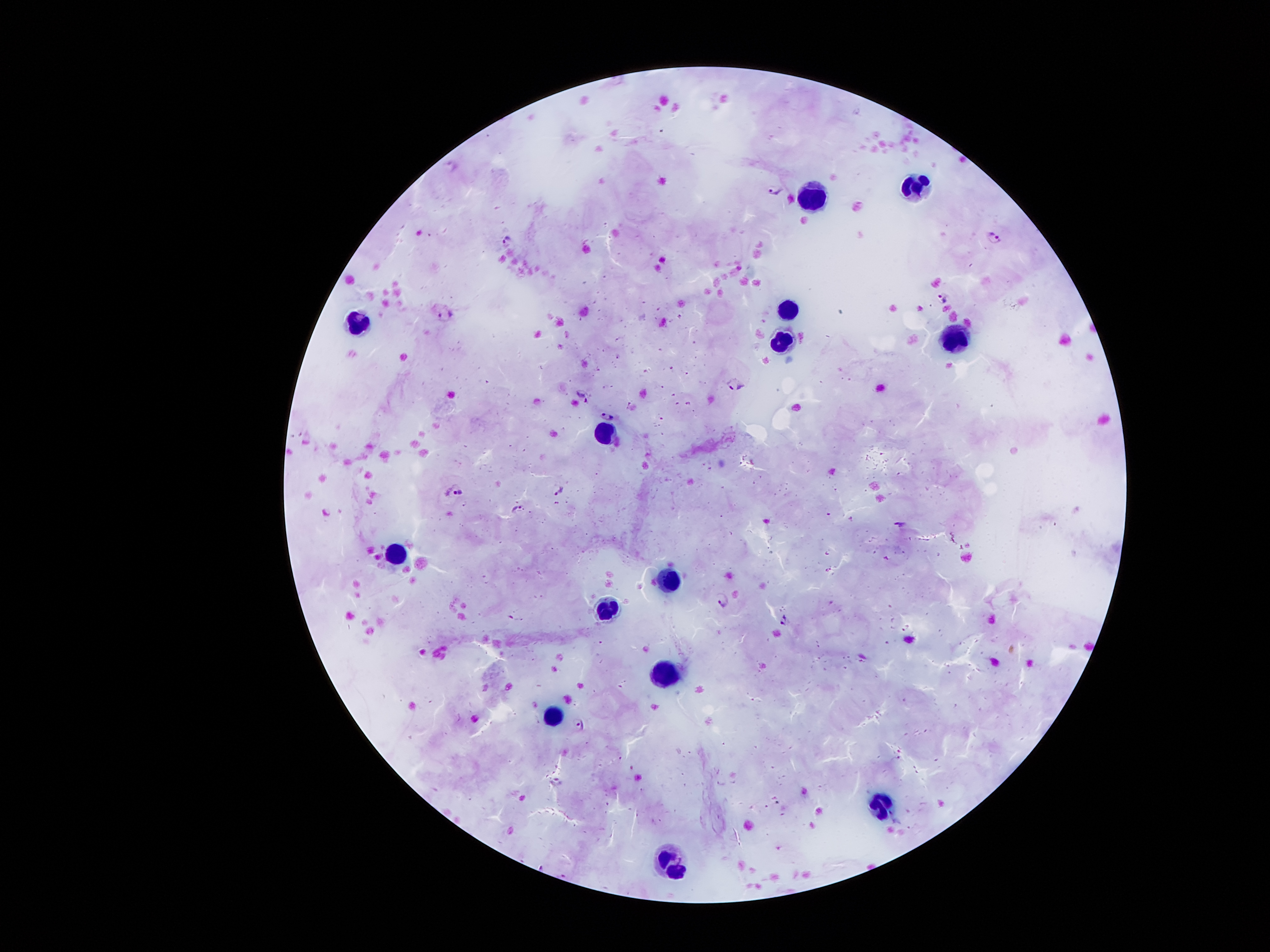
Approximate centers as [x, y] in pixels. Malaria parasite locations: [774, 190], [994, 236], [507, 241], [944, 295], [446, 314], [735, 381], [582, 395], [606, 416], [558, 487], [460, 492], [517, 510], [900, 524], [722, 600], [783, 620], [579, 723], [558, 781]. Leukocyte locations: [916, 189], [814, 193], [788, 312], [357, 325], [783, 337], [954, 337], [604, 435], [398, 556], [671, 576], [605, 607], [667, 676], [555, 715], [881, 806], [668, 867]. Thick blood film. Patient malaria status: infected with Plasmodium falciparum. 100x magnification. Photographed through the microscope eyepiece with a smartphone camera. Single field of view. Giemsa stain. Image is 1270×952 pixels.